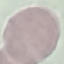
Summary:
  - Malaria status: uninfected
  - Preparation: thin blood film
  - Stain: Giemsa
  - Capture: smartphone through the microscope eyepiece
  - Image type: automatically extracted cell patch, resized to 64 × 64 pixels